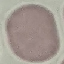

malaria status = uninfected
stain = Giemsa
image type = automatically extracted cell patch, resized to 64 × 64 pixels
capture = smartphone through the microscope eyepiece
preparation = thin smear